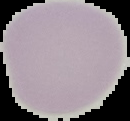 Malaria status: uninfected. From a thin blood film. Image is 130×121 pixels. Cell region segmented out of the field of view; the surrounding area is masked to black.